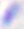

magnification: 400x
modality: photomicrograph
identification: Toxoplasma gondii